Locate every Plasmodium vivax-infected red blood cell.
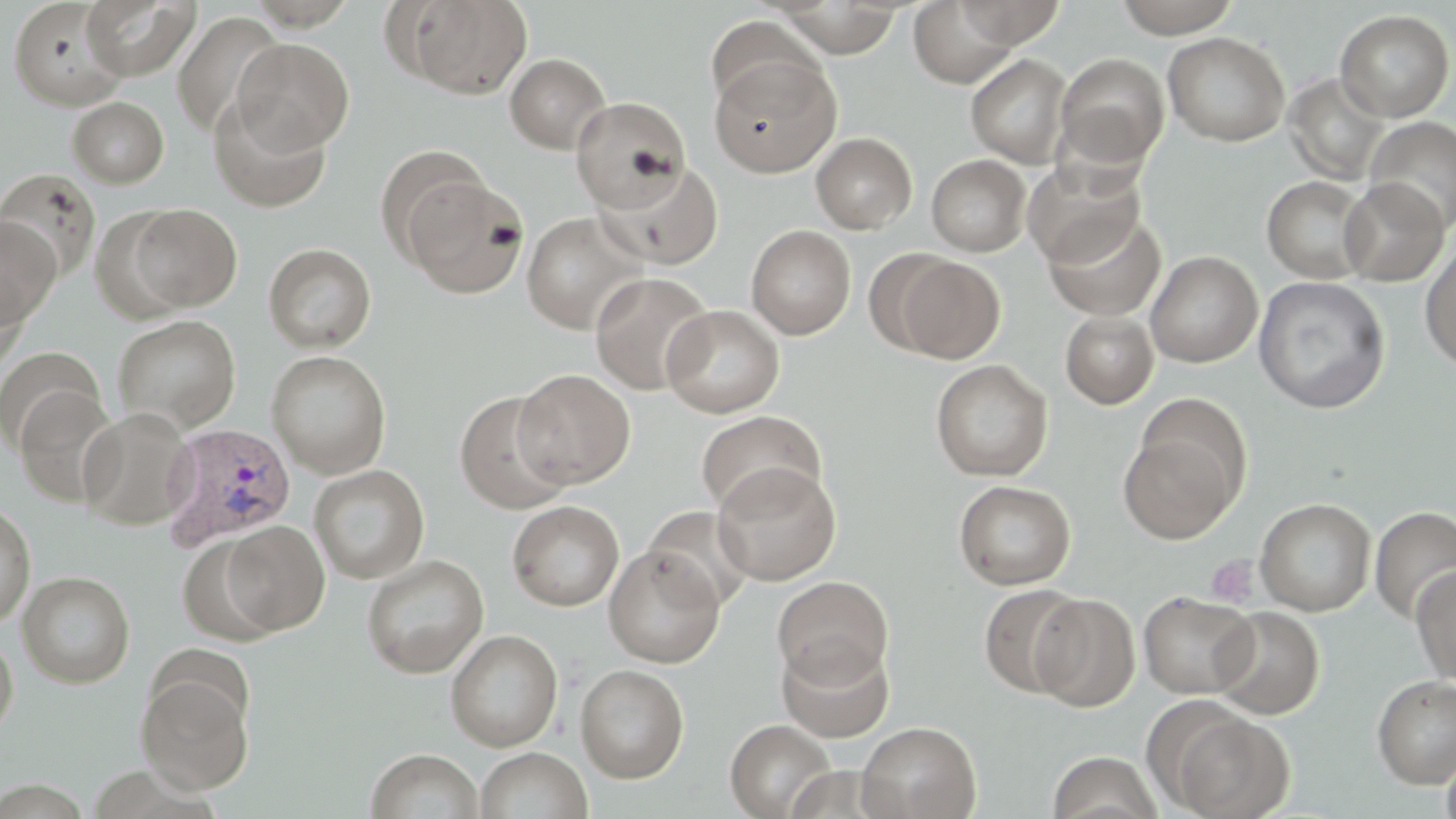
Approximate bounding boxes as named x1/y1/x2/y2 corners in pixels.
Plasmodium vivax-infected red blood cells: (x1=159, y1=423, x2=297, y2=551).

Platelet locations: (x1=1204, y1=553, x2=1261, y2=609). Uninfected red blood cell locations: (x1=79, y1=0, x2=201, y2=80), (x1=909, y1=0, x2=1023, y2=88), (x1=1112, y1=0, x2=1243, y2=37), (x1=8, y1=1, x2=128, y2=110), (x1=396, y1=1, x2=533, y2=99), (x1=954, y1=1, x2=1066, y2=48), (x1=772, y1=2, x2=906, y2=58), (x1=1334, y1=9, x2=1455, y2=122), (x1=172, y1=11, x2=287, y2=139), (x1=703, y1=16, x2=821, y2=114), (x1=1162, y1=32, x2=1290, y2=147), (x1=232, y1=37, x2=354, y2=155), (x1=504, y1=53, x2=611, y2=153), (x1=966, y1=53, x2=1073, y2=167), (x1=1055, y1=53, x2=1169, y2=170), (x1=709, y1=54, x2=840, y2=177), (x1=1284, y1=72, x2=1390, y2=185), (x1=207, y1=95, x2=333, y2=213), (x1=68, y1=96, x2=169, y2=188), (x1=571, y1=97, x2=691, y2=211), (x1=1365, y1=116, x2=1456, y2=233), (x1=811, y1=132, x2=918, y2=234), (x1=374, y1=146, x2=492, y2=262), (x1=927, y1=154, x2=1031, y2=257), (x1=1022, y1=157, x2=1145, y2=268), (x1=595, y1=161, x2=724, y2=270), (x1=0, y1=169, x2=101, y2=283), (x1=401, y1=173, x2=529, y2=299), (x1=1261, y1=175, x2=1374, y2=283), (x1=1339, y1=178, x2=1449, y2=287), (x1=124, y1=203, x2=242, y2=313), (x1=1043, y1=210, x2=1165, y2=322), (x1=521, y1=212, x2=647, y2=334), (x1=0, y1=215, x2=61, y2=330), (x1=746, y1=225, x2=856, y2=339), (x1=1420, y1=237, x2=1456, y2=371), (x1=263, y1=243, x2=376, y2=353), (x1=1145, y1=250, x2=1262, y2=368), (x1=893, y1=256, x2=1005, y2=363), (x1=0, y1=269, x2=29, y2=375), (x1=590, y1=272, x2=715, y2=396), (x1=1253, y1=275, x2=1390, y2=413), (x1=662, y1=305, x2=784, y2=418), (x1=1060, y1=310, x2=1159, y2=409), (x1=111, y1=314, x2=241, y2=436), (x1=0, y1=346, x2=105, y2=454), (x1=266, y1=350, x2=392, y2=478), (x1=931, y1=359, x2=1053, y2=482), (x1=513, y1=369, x2=635, y2=488), (x1=14, y1=387, x2=122, y2=508), (x1=454, y1=390, x2=574, y2=515), (x1=78, y1=407, x2=195, y2=531), (x1=696, y1=409, x2=826, y2=517), (x1=1117, y1=426, x2=1242, y2=543), (x1=712, y1=463, x2=842, y2=585), (x1=309, y1=464, x2=430, y2=584), (x1=954, y1=480, x2=1076, y2=590), (x1=1255, y1=497, x2=1375, y2=616), (x1=0, y1=500, x2=36, y2=626), (x1=507, y1=500, x2=625, y2=611), (x1=642, y1=505, x2=756, y2=612), (x1=1369, y1=506, x2=1456, y2=622), (x1=220, y1=521, x2=330, y2=635), (x1=176, y1=534, x2=284, y2=646), (x1=604, y1=546, x2=726, y2=667), (x1=361, y1=554, x2=489, y2=678), (x1=1411, y1=565, x2=1456, y2=686), (x1=18, y1=571, x2=136, y2=688), (x1=771, y1=575, x2=893, y2=688), (x1=978, y1=582, x2=1089, y2=699), (x1=1138, y1=591, x2=1259, y2=699), (x1=1030, y1=594, x2=1140, y2=711), (x1=1210, y1=606, x2=1325, y2=719), (x1=445, y1=629, x2=564, y2=751), (x1=0, y1=633, x2=18, y2=743), (x1=776, y1=639, x2=894, y2=743), (x1=575, y1=664, x2=689, y2=784), (x1=136, y1=674, x2=253, y2=794), (x1=1372, y1=675, x2=1456, y2=788), (x1=1163, y1=708, x2=1293, y2=819), (x1=725, y1=719, x2=836, y2=818), (x1=857, y1=721, x2=981, y2=819), (x1=1440, y1=742, x2=1456, y2=819), (x1=475, y1=747, x2=592, y2=819), (x1=366, y1=749, x2=484, y2=819), (x1=1047, y1=750, x2=1163, y2=819). Slide-level diagnosis: Plasmodium vivax. Light microscopy. Single field of view. Captured at 1000x magnification. Image is 1456×819 pixels. May-Grünwald-Giemsa-stained preparation. Thin blood smear.